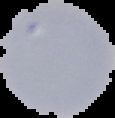
preparation = thin blood film
image type = segmented cell region on a black background
malaria status = uninfected
image size = 115×118 pixels